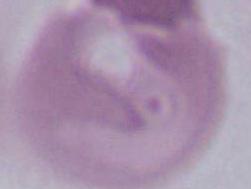
magnification = 1000x
identification = red blood cell
modality = photomicrograph